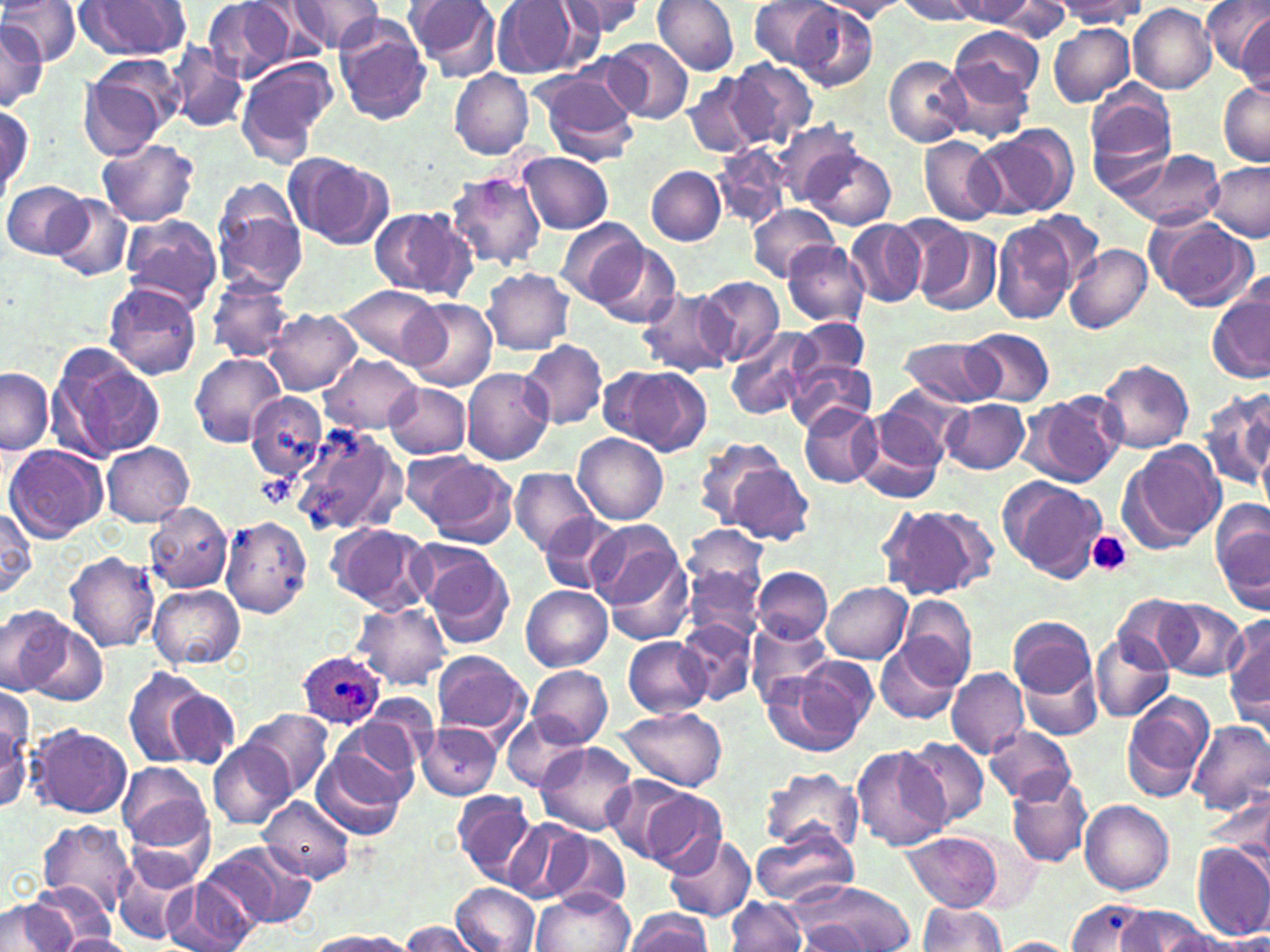
{
  "slide_level_diagnosis": "Plasmodium ovale",
  "platelet_locations": "approximate bounding boxes as (x1, y1, x2, y2) in pixels: (256, 472, 295, 507), (1086, 530, 1132, 576)",
  "plasmodium_ovale_infected_red_blood_cell_locations": "approximate bounding boxes as (x1, y1, x2, y2) in pixels: (298, 650, 386, 730)",
  "image_size": "1270×952 pixels",
  "magnification": "1000x",
  "modality": "optical microscopy",
  "uninfected_red_blood_cell_locations": "approximate bounding boxes as (x1, y1, x2, y2) in pixels: (0, 0, 80, 65), (202, 0, 294, 83), (287, 0, 385, 53), (402, 0, 503, 79), (490, 0, 586, 80), (556, 0, 648, 41), (651, 0, 740, 76), (819, 0, 913, 22), (895, 0, 976, 23), (947, 0, 1040, 25), (980, 0, 1072, 38), (1203, 0, 1270, 76), (76, 1, 191, 59), (748, 1, 835, 68), (1057, 1, 1145, 29), (789, 2, 877, 92), (256, 4, 337, 61), (1128, 4, 1215, 94), (1234, 10, 1269, 92), (332, 18, 433, 126), (0, 21, 46, 110), (1048, 23, 1134, 106), (949, 25, 1042, 107), (604, 38, 693, 122), (166, 46, 248, 131), (884, 55, 973, 147), (234, 57, 337, 162), (726, 58, 816, 148), (77, 65, 174, 160), (938, 66, 1032, 143), (535, 67, 640, 165), (450, 70, 533, 158), (683, 74, 764, 159), (1218, 78, 1270, 166), (1085, 80, 1176, 171), (1, 103, 32, 196), (771, 118, 869, 207), (977, 127, 1076, 219), (918, 135, 1002, 225), (96, 139, 200, 227), (712, 146, 792, 230), (805, 146, 895, 229), (1113, 147, 1224, 231), (518, 151, 614, 234), (285, 154, 391, 248), (1205, 161, 1268, 242), (647, 166, 726, 246), (445, 172, 546, 270), (212, 178, 309, 296), (3, 181, 91, 260), (50, 196, 133, 282), (745, 205, 840, 283), (368, 206, 477, 301), (1023, 210, 1104, 289), (1145, 214, 1257, 311), (118, 215, 223, 311), (557, 218, 652, 308), (846, 219, 926, 308), (992, 219, 1081, 324), (911, 224, 1002, 316), (582, 240, 681, 328), (780, 240, 870, 325), (1064, 243, 1152, 334), (481, 269, 576, 354), (206, 275, 294, 362), (696, 276, 783, 367), (103, 282, 202, 379), (334, 285, 445, 368), (1208, 287, 1270, 384), (637, 288, 737, 377), (403, 298, 498, 391), (264, 309, 363, 396), (791, 316, 870, 384), (726, 327, 817, 420), (964, 329, 1054, 407), (899, 335, 1001, 407), (520, 340, 607, 431), (45, 342, 165, 464), (189, 352, 285, 446), (321, 354, 420, 431), (1097, 358, 1195, 453), (786, 360, 877, 437), (603, 366, 709, 454), (0, 367, 53, 455), (461, 367, 555, 465), (384, 383, 471, 457), (875, 383, 969, 468), (1202, 388, 1270, 494), (246, 391, 327, 482), (1027, 391, 1124, 487), (942, 398, 1029, 475), (256, 399, 367, 511), (799, 403, 882, 488), (854, 409, 949, 504), (293, 423, 405, 538), (574, 433, 668, 524), (693, 436, 787, 528), (1123, 441, 1225, 549), (101, 443, 195, 526), (4, 445, 107, 544), (416, 454, 517, 546), (722, 457, 814, 545), (510, 467, 599, 557), (1003, 478, 1105, 581), (1212, 498, 1270, 614), (145, 502, 233, 593), (879, 502, 996, 601), (0, 505, 36, 601), (537, 513, 623, 594), (219, 515, 313, 618), (327, 523, 432, 614), (683, 523, 769, 613), (596, 534, 694, 644), (415, 543, 512, 643), (63, 552, 160, 653), (682, 561, 763, 645), (753, 567, 831, 643), (823, 582, 912, 663), (148, 584, 246, 670), (520, 585, 611, 671), (1111, 595, 1200, 672), (901, 596, 976, 686), (1155, 599, 1247, 680), (354, 603, 451, 689), (0, 609, 84, 700), (1007, 615, 1097, 703), (1225, 615, 1270, 726), (674, 618, 757, 705), (747, 621, 832, 708), (1090, 631, 1174, 723), (623, 636, 711, 718), (876, 638, 962, 725), (430, 650, 530, 738), (1015, 654, 1102, 744), (763, 662, 874, 757), (526, 665, 612, 748), (946, 666, 1029, 758), (123, 669, 229, 770), (165, 689, 237, 767), (1, 691, 33, 811), (1121, 691, 1210, 800), (364, 695, 437, 769), (243, 708, 334, 799), (617, 708, 729, 791), (503, 714, 589, 792), (333, 718, 424, 805), (1186, 721, 1270, 817), (28, 724, 132, 818), (415, 724, 504, 800), (983, 727, 1076, 803), (903, 736, 991, 828), (208, 742, 293, 829), (534, 742, 641, 835), (311, 744, 408, 841), (850, 744, 948, 851), (117, 762, 214, 850), (761, 766, 863, 854), (600, 774, 697, 864), (1007, 777, 1092, 867), (642, 789, 730, 875), (451, 791, 541, 886), (258, 797, 355, 884), (1079, 800, 1174, 894), (121, 802, 217, 891), (38, 819, 136, 913), (502, 819, 592, 906), (547, 829, 631, 909), (751, 829, 858, 908), (663, 832, 755, 922), (903, 833, 1003, 910), (205, 842, 318, 931), (1190, 843, 1270, 941), (111, 852, 201, 946), (166, 875, 256, 952), (786, 880, 912, 952), (29, 881, 114, 946), (452, 883, 539, 952), (533, 889, 633, 952), (726, 896, 805, 951), (6, 898, 77, 951), (1067, 898, 1155, 950), (915, 901, 1008, 951), (1115, 907, 1213, 950), (625, 909, 714, 952), (798, 919, 869, 948), (400, 921, 478, 952), (1153, 929, 1245, 952), (306, 931, 412, 951), (59, 933, 133, 952), (996, 937, 1078, 952)",
  "field_of_view": "single",
  "stain": "May-Grünwald-Giemsa",
  "preparation": "thin blood smear"
}